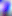

magnification: 400x
modality: photomicrograph
identification: Toxoplasma gondii